Outline each uninfected red blood cell.
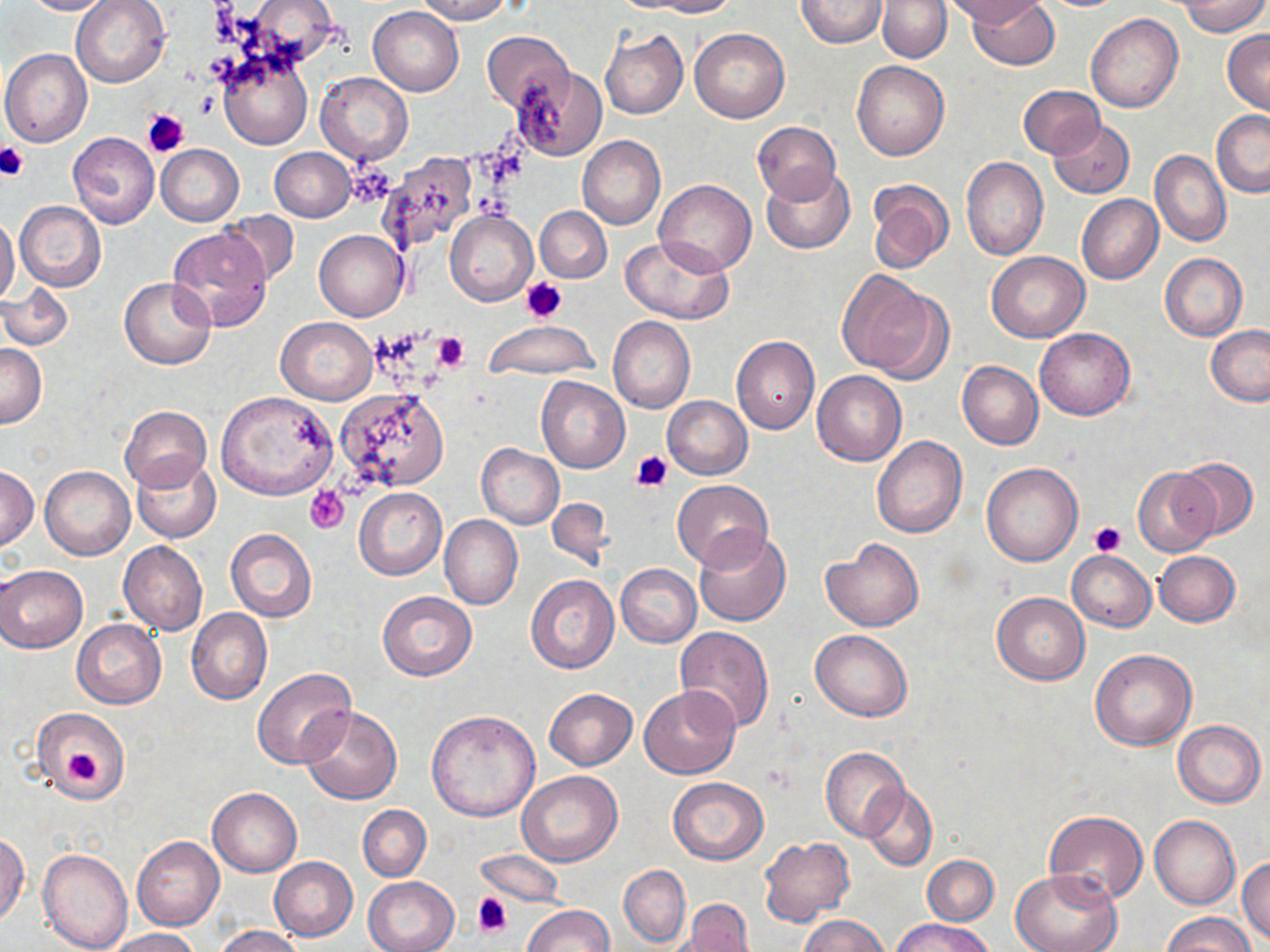

Approximate bounding boxes as (x1,y1)-(x2,y2) corner pairs in pixels.
Uninfected red blood cells: (21,0)-(118,16), (71,0)-(170,89), (413,0)-(516,23), (640,0)-(738,16), (795,0)-(886,48), (944,0)-(1045,26), (966,0)-(1059,71), (877,1)-(951,63), (1174,1)-(1269,37), (368,6)-(463,96), (1086,13)-(1183,114), (688,27)-(790,123), (600,28)-(688,119), (1223,29)-(1270,115), (482,31)-(573,111), (1,48)-(91,147), (219,50)-(311,149), (851,60)-(948,160), (513,66)-(607,161), (316,72)-(413,165), (1017,86)-(1104,159), (1211,109)-(1270,197), (1049,118)-(1134,199), (753,121)-(841,205), (68,132)-(160,229), (578,136)-(666,229), (155,144)-(244,226), (270,148)-(356,221), (1150,150)-(1231,247), (376,151)-(483,254), (961,157)-(1048,261), (762,165)-(855,254), (655,179)-(757,275), (865,179)-(954,274), (1077,194)-(1163,283), (15,201)-(106,292), (535,205)-(612,283), (445,208)-(539,306), (219,210)-(299,288), (0,216)-(20,307), (165,227)-(273,332), (314,230)-(408,321), (620,235)-(734,324), (987,251)-(1089,342), (1160,253)-(1246,341), (837,269)-(947,379), (118,277)-(215,369), (1,282)-(73,351), (608,316)-(695,414), (275,317)-(378,404), (482,321)-(599,380), (1205,326)-(1270,406), (1034,328)-(1135,420), (731,335)-(819,434), (0,343)-(46,428), (957,361)-(1043,450), (813,370)-(907,466), (537,376)-(629,473), (335,388)-(450,492), (216,391)-(338,500), (662,395)-(753,479), (120,405)-(211,492), (872,435)-(965,538), (475,444)-(564,529), (133,454)-(221,542), (1173,456)-(1260,541), (981,462)-(1084,566), (0,466)-(40,550), (41,466)-(134,560), (1133,466)-(1219,558), (673,481)-(773,569), (354,487)-(447,580), (544,497)-(614,571), (439,515)-(522,609), (225,528)-(317,622), (693,528)-(790,627), (823,538)-(924,632), (119,542)-(207,635), (1068,550)-(1156,632), (1153,551)-(1240,626), (0,564)-(87,652), (615,564)-(701,646), (526,574)-(619,674), (378,590)-(476,680), (992,592)-(1090,684), (186,608)-(272,705), (71,620)-(166,708), (675,626)-(775,732), (810,629)-(913,721), (1090,649)-(1197,750), (252,667)-(357,770), (638,685)-(741,779), (544,688)-(637,770), (300,706)-(402,805), (33,708)-(130,802), (427,710)-(541,822), (1173,719)-(1265,807), (821,747)-(908,840), (516,772)-(621,867), (668,777)-(769,864), (861,784)-(937,871), (208,787)-(301,876), (360,804)-(440,952), (358,805)-(431,881), (1044,811)-(1148,902), (1150,814)-(1240,909), (0,833)-(29,925), (132,836)-(224,931), (758,836)-(854,926), (38,847)-(134,952), (476,850)-(565,908), (922,855)-(999,925), (269,857)-(358,941), (1237,857)-(1270,944), (618,865)-(691,949), (1013,869)-(1121,952), (362,876)-(458,952), (677,900)-(756,952), (522,905)-(613,952), (1164,913)-(1255,952), (799,914)-(890,952), (891,916)-(996,951), (214,926)-(304,952), (103,928)-(202,951).

Platelet locations: (141,106)-(190,158), (0,141)-(29,181), (347,160)-(394,208), (521,275)-(568,321), (433,332)-(469,370), (632,451)-(673,492), (304,485)-(350,532), (1091,520)-(1127,556), (63,747)-(102,786), (472,891)-(512,938). Slide-level diagnosis: negative for blood parasites. Single field of view. Captured at 1000x magnification. Light microscopy. Image is 1270×952 pixels. Thin blood smear. May-Grünwald-Giemsa-stained preparation.